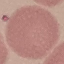
{
  "result": "no malaria parasites detected",
  "image_type": "cell patch, automatically extracted from a larger field of view and resized to 64 × 64 pixels",
  "stain": "Giemsa",
  "preparation": "thin smear",
  "capture": "smartphone camera at the microscope eyepiece"
}